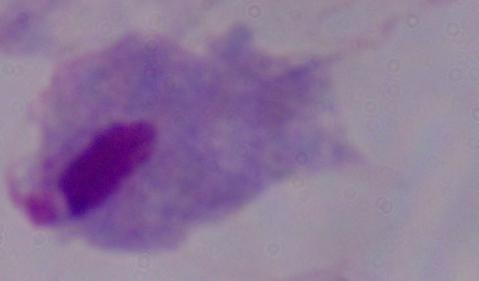

A trichomonad is shown. 1000x magnification. Photomicrograph.